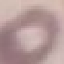
Summary:
  - Result: negative for malaria parasites
  - Image type: cell patch, automatically extracted from a larger field of view and resized to 64 × 64 pixels
  - Capture: smartphone through the microscope eyepiece
  - Preparation: thin blood smear
  - Stain: Giemsa